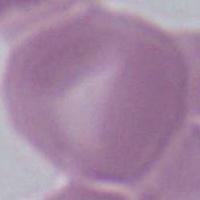

Summary:
  - Modality: micrograph
  - Identification: erythrocyte
  - Magnification: 1000x